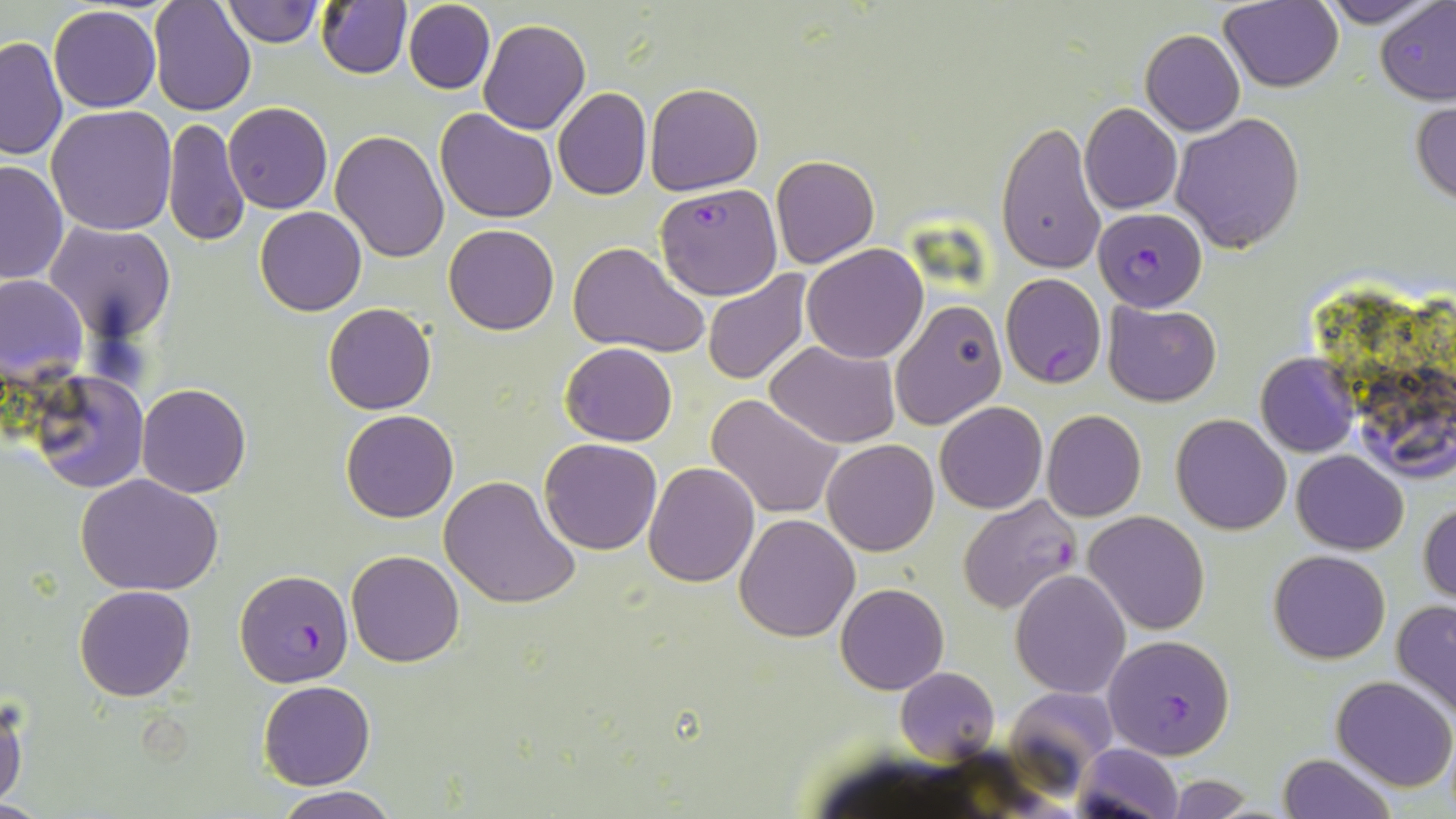

{
  "slide_level_diagnosis": "Plasmodium falciparum",
  "uninfected_red_blood_cell_locations": "approximate bounding boxes as [x1, y1, x2, y2] in pixels: [148, 0, 256, 117], [221, 0, 322, 46], [1314, 0, 1443, 27], [315, 1, 411, 80], [402, 1, 496, 93], [1218, 1, 1343, 92], [1376, 4, 1456, 104], [49, 6, 161, 111], [479, 18, 591, 135], [1139, 29, 1246, 136], [0, 35, 68, 161], [644, 82, 763, 195], [554, 87, 653, 200], [1412, 96, 1456, 209], [223, 102, 332, 215], [1080, 102, 1182, 214], [47, 105, 177, 236], [435, 107, 559, 223], [1171, 113, 1306, 253], [165, 117, 249, 248], [996, 120, 1107, 276], [331, 130, 450, 263], [770, 154, 879, 269], [0, 159, 68, 284], [255, 206, 367, 317], [45, 222, 175, 340], [443, 223, 560, 336], [566, 241, 708, 358], [802, 244, 929, 364], [704, 269, 816, 386], [0, 274, 89, 387], [888, 300, 1007, 428], [1102, 301, 1222, 406], [323, 302, 436, 415], [766, 340, 900, 449], [560, 342, 677, 447], [1256, 352, 1360, 456], [28, 369, 150, 494], [136, 383, 252, 498], [706, 394, 843, 520], [935, 401, 1046, 514], [340, 409, 458, 523], [1041, 409, 1147, 521], [1171, 413, 1291, 534], [538, 438, 663, 555], [823, 439, 939, 555], [1292, 450, 1408, 555], [644, 462, 760, 586], [74, 473, 224, 596], [441, 475, 581, 610], [1420, 503, 1456, 603], [1084, 511, 1210, 634], [734, 513, 860, 642], [1267, 549, 1391, 664], [347, 550, 464, 667], [1010, 569, 1130, 699], [835, 583, 949, 695], [75, 584, 196, 701], [1391, 601, 1456, 720], [895, 667, 1000, 763], [1331, 675, 1455, 790], [259, 681, 375, 790], [0, 697, 27, 809], [1074, 743, 1183, 818], [1277, 754, 1396, 818], [1167, 775, 1256, 816], [270, 787, 404, 819]",
  "stain": "May-Grünwald-Giemsa",
  "field_of_view": "single",
  "magnification": "1000x",
  "modality": "light microscopy",
  "preparation": "thin blood smear",
  "image_size": "1456×819 pixels",
  "plasmodium_falciparum_infected_red_blood_cell_locations": "approximate bounding boxes as [x1, y1, x2, y2] in pixels: [655, 182, 783, 300], [1093, 207, 1207, 311], [999, 272, 1107, 388], [956, 493, 1084, 615], [234, 567, 355, 680], [1105, 634, 1235, 760]"
}